Give the extent of all Plasmodium vivax-infected red blood cells.
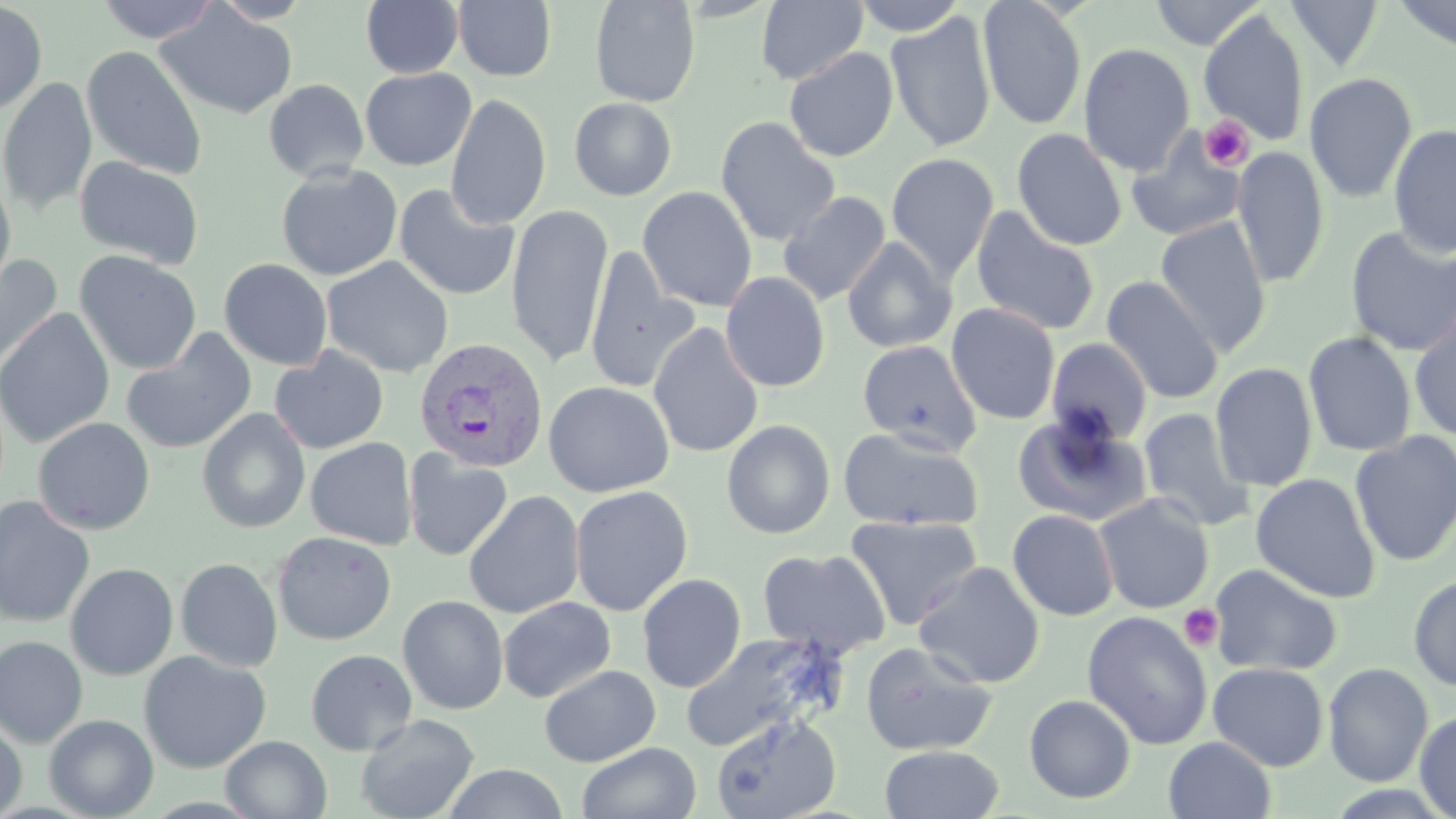
Approximate bounding boxes as named x1/y1/x2/y2 corners in pixels.
Plasmodium vivax-infected red blood cells: (x1=414, y1=338, x2=550, y2=474).

Summary:
  - Uninfected red blood cell locations: (x1=95, y1=0, x2=220, y2=43), (x1=209, y1=0, x2=315, y2=25), (x1=360, y1=0, x2=464, y2=78), (x1=589, y1=0, x2=701, y2=107), (x1=851, y1=0, x2=969, y2=36), (x1=977, y1=0, x2=1088, y2=130), (x1=1148, y1=0, x2=1266, y2=50), (x1=1285, y1=0, x2=1384, y2=71), (x1=1392, y1=0, x2=1456, y2=54), (x1=0, y1=1, x2=48, y2=114), (x1=453, y1=1, x2=557, y2=82), (x1=756, y1=1, x2=868, y2=86), (x1=155, y1=3, x2=298, y2=120), (x1=885, y1=11, x2=996, y2=153), (x1=1199, y1=11, x2=1308, y2=145), (x1=1079, y1=43, x2=1194, y2=174), (x1=82, y1=45, x2=207, y2=180), (x1=783, y1=47, x2=899, y2=162), (x1=360, y1=67, x2=476, y2=170), (x1=1303, y1=72, x2=1418, y2=204), (x1=0, y1=77, x2=98, y2=215), (x1=263, y1=79, x2=369, y2=182), (x1=445, y1=93, x2=551, y2=229), (x1=569, y1=97, x2=677, y2=201), (x1=715, y1=115, x2=840, y2=246), (x1=1388, y1=123, x2=1456, y2=256), (x1=1011, y1=128, x2=1128, y2=250), (x1=1125, y1=128, x2=1248, y2=242), (x1=1231, y1=146, x2=1330, y2=287), (x1=886, y1=152, x2=999, y2=282), (x1=74, y1=156, x2=205, y2=270), (x1=276, y1=164, x2=403, y2=281), (x1=0, y1=170, x2=16, y2=298), (x1=394, y1=183, x2=520, y2=301), (x1=637, y1=186, x2=757, y2=312), (x1=778, y1=191, x2=892, y2=306), (x1=505, y1=204, x2=613, y2=368), (x1=971, y1=205, x2=1101, y2=337), (x1=1155, y1=216, x2=1271, y2=356), (x1=1344, y1=226, x2=1456, y2=356), (x1=842, y1=237, x2=957, y2=353), (x1=74, y1=250, x2=202, y2=375), (x1=583, y1=250, x2=698, y2=394), (x1=0, y1=254, x2=63, y2=369), (x1=321, y1=256, x2=453, y2=377), (x1=219, y1=258, x2=333, y2=370), (x1=720, y1=272, x2=830, y2=393), (x1=1101, y1=276, x2=1223, y2=404), (x1=946, y1=303, x2=1061, y2=425), (x1=0, y1=307, x2=115, y2=448), (x1=1408, y1=309, x2=1456, y2=442), (x1=648, y1=322, x2=764, y2=458), (x1=121, y1=329, x2=257, y2=455), (x1=1303, y1=331, x2=1417, y2=457), (x1=1045, y1=337, x2=1153, y2=447), (x1=857, y1=340, x2=982, y2=454), (x1=269, y1=346, x2=389, y2=454), (x1=286, y1=346, x2=405, y2=551), (x1=1210, y1=362, x2=1317, y2=492), (x1=543, y1=380, x2=674, y2=497), (x1=1138, y1=407, x2=1255, y2=532), (x1=197, y1=408, x2=310, y2=533), (x1=1012, y1=411, x2=1152, y2=527), (x1=33, y1=417, x2=156, y2=535), (x1=720, y1=419, x2=836, y2=539), (x1=837, y1=426, x2=984, y2=531), (x1=1349, y1=431, x2=1456, y2=566), (x1=305, y1=437, x2=418, y2=550), (x1=403, y1=448, x2=513, y2=561), (x1=1250, y1=472, x2=1381, y2=602), (x1=569, y1=485, x2=693, y2=616), (x1=463, y1=489, x2=585, y2=619), (x1=1094, y1=493, x2=1214, y2=613), (x1=0, y1=495, x2=95, y2=628), (x1=1007, y1=509, x2=1119, y2=621), (x1=844, y1=514, x2=983, y2=631), (x1=272, y1=531, x2=396, y2=645), (x1=757, y1=547, x2=890, y2=658), (x1=175, y1=557, x2=283, y2=672), (x1=913, y1=561, x2=1045, y2=688), (x1=65, y1=563, x2=179, y2=680), (x1=1209, y1=563, x2=1343, y2=677), (x1=637, y1=573, x2=746, y2=692), (x1=1408, y1=575, x2=1456, y2=692), (x1=397, y1=594, x2=509, y2=714), (x1=498, y1=596, x2=616, y2=703), (x1=1082, y1=610, x2=1213, y2=750), (x1=678, y1=631, x2=844, y2=753), (x1=0, y1=636, x2=88, y2=748), (x1=859, y1=641, x2=998, y2=756), (x1=305, y1=648, x2=418, y2=755), (x1=138, y1=650, x2=271, y2=774), (x1=1208, y1=662, x2=1329, y2=771), (x1=1323, y1=662, x2=1434, y2=787), (x1=539, y1=664, x2=660, y2=767), (x1=1024, y1=694, x2=1136, y2=804), (x1=1414, y1=710, x2=1456, y2=819), (x1=355, y1=713, x2=479, y2=819), (x1=711, y1=713, x2=842, y2=818), (x1=44, y1=714, x2=158, y2=818), (x1=0, y1=718, x2=28, y2=818), (x1=220, y1=735, x2=331, y2=818), (x1=1163, y1=736, x2=1276, y2=819), (x1=577, y1=742, x2=701, y2=819), (x1=879, y1=744, x2=1005, y2=819), (x1=441, y1=764, x2=570, y2=819)
  - Platelet locations: (x1=1199, y1=116, x2=1254, y2=170), (x1=1178, y1=603, x2=1223, y2=651)
  - Slide-level diagnosis: Plasmodium vivax
  - Magnification: 1000x
  - Stain: May-Grünwald-Giemsa
  - Modality: optical microscopy
  - Field of view: one of a larger specimen
  - Preparation: thin blood smear
  - Image size: 1456×819 pixels